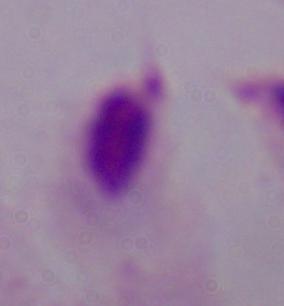
Summary:
  - Identification: trichomonad
  - Magnification: 1000x
  - Modality: photomicrograph